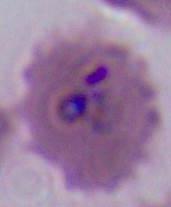

Summary:
  - Modality: photomicrograph
  - Identification: Plasmodium
  - Magnification: 400x or 1000x